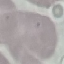

Summary:
  - Malaria status: uninfected
  - Preparation: thin smear
  - Capture: smartphone camera at the microscope eyepiece
  - Stain: Giemsa
  - Image type: cell patch, automatically extracted from a larger field of view and resized to 64 × 64 pixels